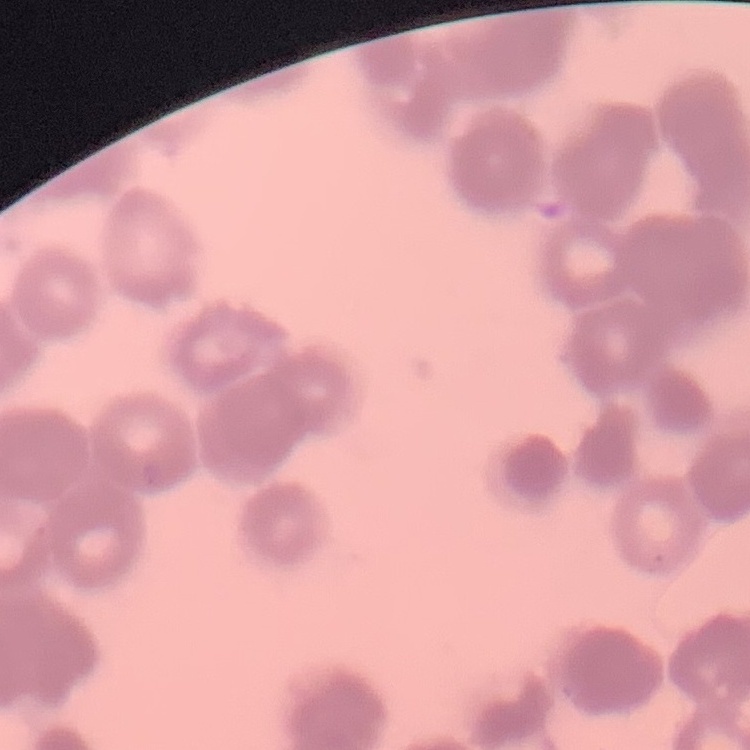

Summary:
  - Erythrocyte morphology: rouleaux formation
  - Image type: square crop of a larger photomicrograph
  - Preparation: thin blood film
  - Stain: Field's or Giemsa